Locate every blood parasite and identify its species.
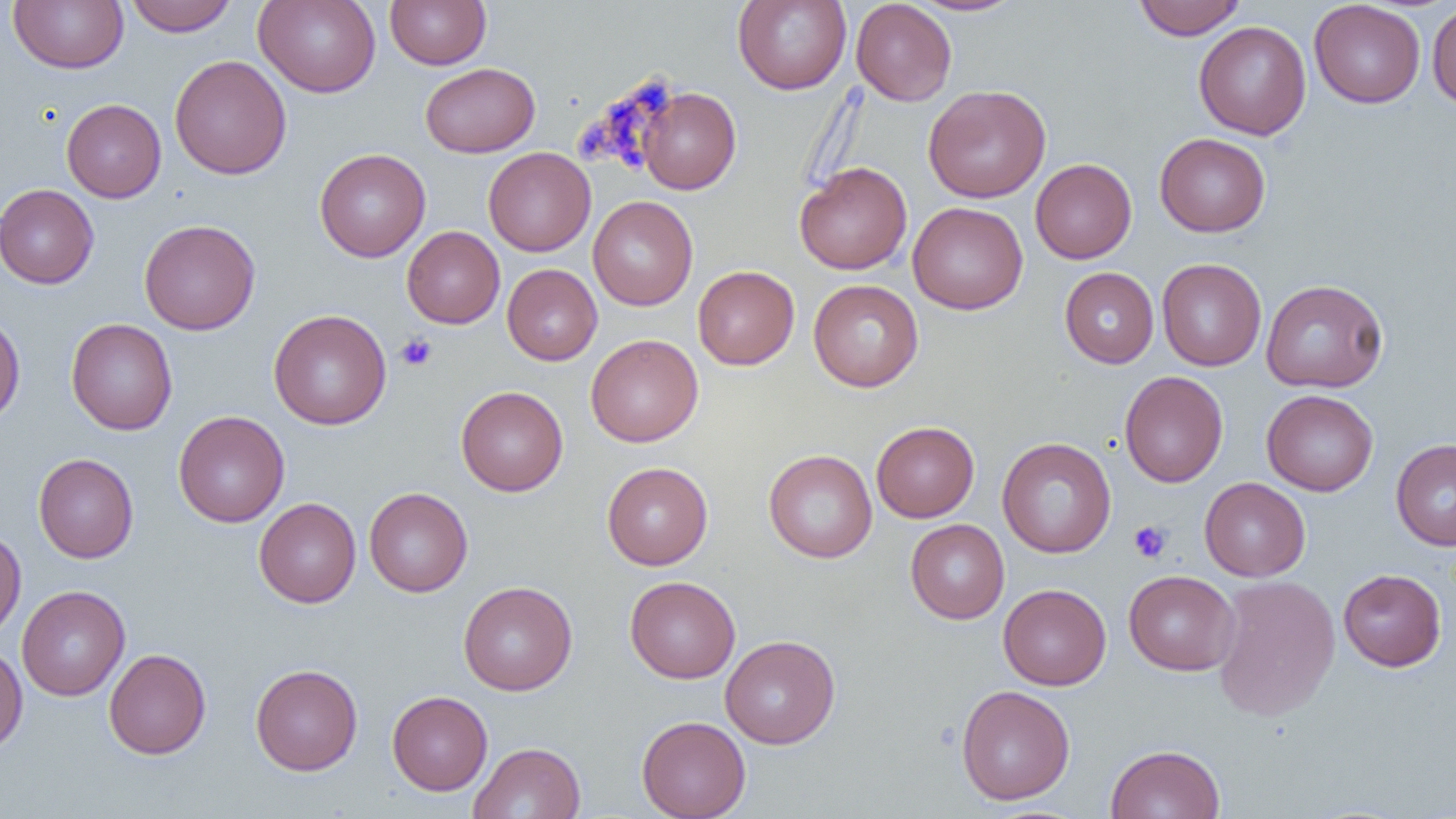
No blood parasites observed.

slide-level diagnosis = no evidence of blood parasites
preparation = thin blood smear
uninfected red blood cell locations = approximate bounding boxes as (x1,y1)-(x2,y2) corner pairs in pixels: (9,0)-(128,73), (125,0)-(237,36), (254,0)-(381,97), (385,0)-(491,70), (732,0)-(851,94), (851,0)-(957,106), (908,0)-(1026,16), (1133,0)-(1245,40), (1309,1)-(1426,108), (1426,3)-(1456,109), (1193,21)-(1311,140), (169,54)-(292,180), (419,63)-(540,157), (923,84)-(1051,203), (638,87)-(741,194), (61,98)-(166,202), (1155,133)-(1271,237), (483,147)-(595,256), (314,148)-(431,262), (1030,158)-(1137,264), (795,161)-(912,275), (0,184)-(99,289), (587,195)-(698,310), (908,202)-(1028,315), (139,219)-(260,335), (402,226)-(505,328), (1157,258)-(1267,371), (502,264)-(602,365), (693,265)-(799,370), (1155,265)-(1389,375), (1059,267)-(1159,368), (808,279)-(924,392), (1260,279)-(1389,393), (268,309)-(392,430), (0,313)-(25,426), (65,318)-(178,435), (585,334)-(703,447), (1119,371)-(1228,487), (456,385)-(568,496), (1262,389)-(1378,496), (173,411)-(289,527), (871,421)-(980,522), (997,437)-(1116,558), (1391,438)-(1456,551), (763,449)-(877,563), (33,453)-(138,563), (602,461)-(713,570), (1199,477)-(1310,581), (363,487)-(473,597), (254,498)-(361,607), (905,519)-(1009,624), (0,529)-(26,639), (1338,569)-(1447,671), (1123,570)-(1240,676), (1212,575)-(1340,721), (625,576)-(740,683), (458,581)-(577,696), (998,583)-(1111,690), (17,585)-(130,701), (720,634)-(840,749), (0,643)-(27,755), (104,649)-(211,759), (250,663)-(363,775), (956,685)-(1075,805), (387,690)-(493,795), (636,715)-(751,819), (468,742)-(585,818), (1105,744)-(1226,819)
platelet locations = approximate bounding boxes as (x1,y1)-(x2,y2) corner pairs in pixels: (637,70)-(676,115), (609,96)-(634,129), (575,121)-(613,161), (611,127)-(642,172), (395,333)-(437,372), (1129,520)-(1172,563)
image size = 1456×819 pixels
magnification = 1000x
modality = optical microscopy
field of view = single